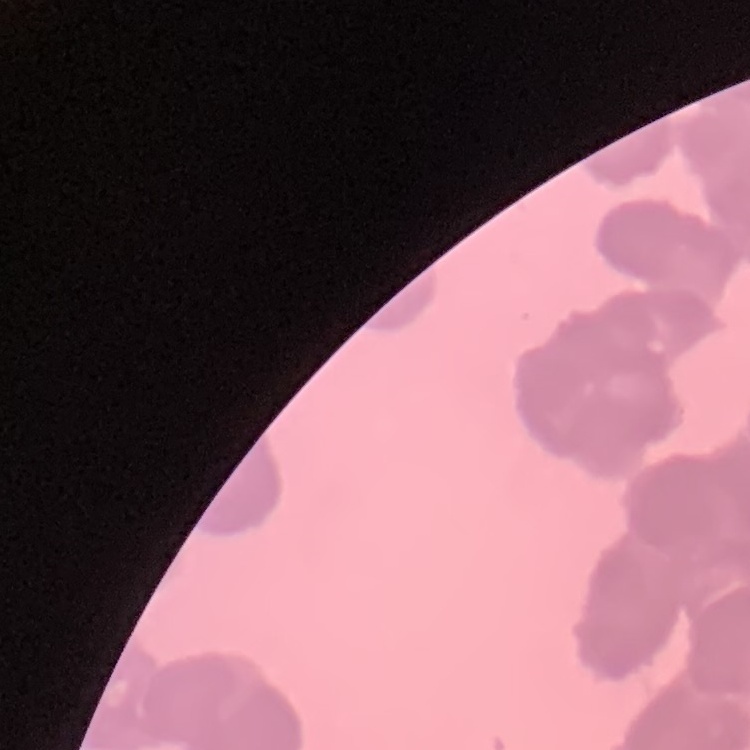
The red blood cells show rouleaux formation. Square crop of a larger photomicrograph. Thin peripheral smear. Stained with either Field's or Giemsa.